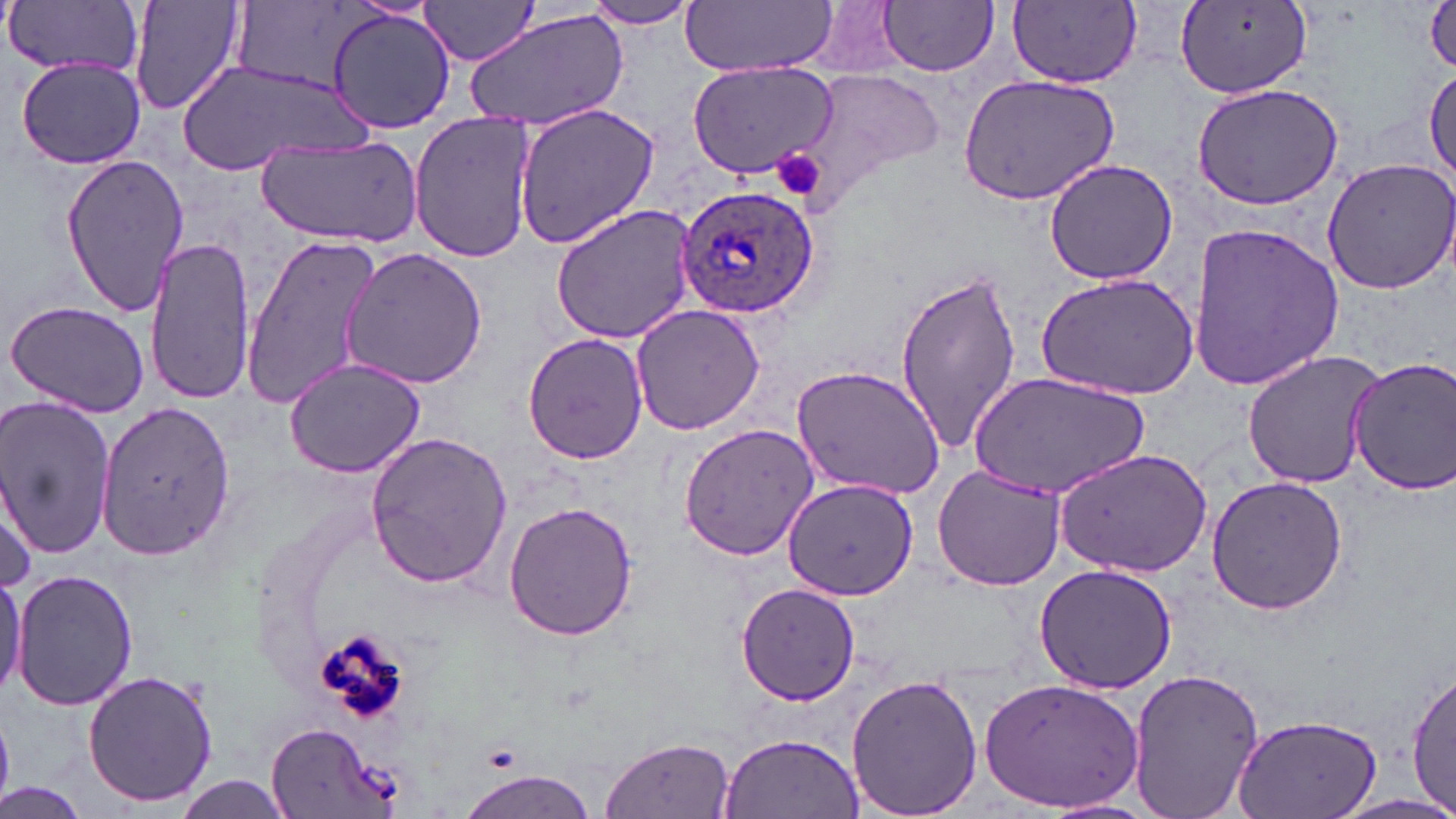
slide-level diagnosis = Plasmodium ovale
field of view = single
platelet locations = approximate bounding boxes as (x1, y1, x2, y2) in pixels: (771, 150, 827, 198)
Plasmodium ovale-infected red blood cell locations = approximate bounding boxes as (x1, y1, x2, y2) in pixels: (675, 183, 819, 318)
preparation = thin blood film
magnification = 1000x
modality = optical microscopy
uninfected red blood cell locations = approximate bounding boxes as (x1, y1, x2, y2) in pixels: (127, 0, 245, 117), (682, 0, 838, 76), (797, 0, 917, 78), (1424, 0, 1456, 73), (5, 1, 144, 81), (419, 1, 543, 66), (579, 1, 703, 30), (879, 1, 998, 75), (1012, 2, 1142, 87), (1177, 2, 1314, 97), (464, 7, 630, 132), (326, 8, 456, 133), (16, 58, 149, 169), (685, 62, 834, 180), (173, 63, 371, 175), (1425, 64, 1456, 186), (796, 69, 948, 206), (957, 74, 1120, 205), (1191, 82, 1345, 210), (511, 101, 661, 250), (406, 114, 537, 263), (255, 134, 422, 247), (61, 153, 189, 316), (1044, 158, 1177, 285), (1322, 158, 1456, 293), (549, 203, 700, 345), (1185, 221, 1344, 393), (240, 235, 380, 412), (144, 238, 256, 406), (339, 246, 487, 390), (894, 267, 1024, 453), (1036, 272, 1199, 398), (5, 300, 152, 419), (630, 304, 766, 435), (522, 333, 651, 463), (1242, 348, 1388, 489), (282, 355, 427, 478), (1346, 355, 1456, 498), (791, 365, 947, 500), (968, 370, 1145, 501), (0, 399, 119, 563), (95, 400, 237, 565), (679, 424, 821, 560), (364, 430, 514, 591), (1054, 447, 1213, 576), (931, 465, 1065, 592), (1206, 475, 1351, 616), (0, 477, 37, 598), (782, 477, 919, 602), (504, 501, 639, 641), (1033, 563, 1177, 693), (0, 567, 25, 704), (12, 568, 138, 710), (738, 580, 860, 705), (1126, 666, 1264, 819), (83, 668, 220, 808), (1407, 669, 1455, 814), (845, 673, 983, 818), (982, 676, 1143, 815), (1231, 709, 1382, 819), (267, 724, 395, 818), (718, 730, 864, 819), (600, 736, 735, 819), (454, 767, 599, 819), (172, 775, 295, 819), (0, 784, 87, 819)
stain = May-Grünwald-Giemsa
image size = 1456×819 pixels